Report the malaria status of this cell.
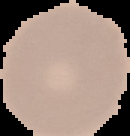

It is uninfected.

{
  "image_size": "130×136 pixels",
  "image_type": "segmented cell region with the area outside set to black",
  "preparation": "thin blood film"
}